Name the blood parasite species.
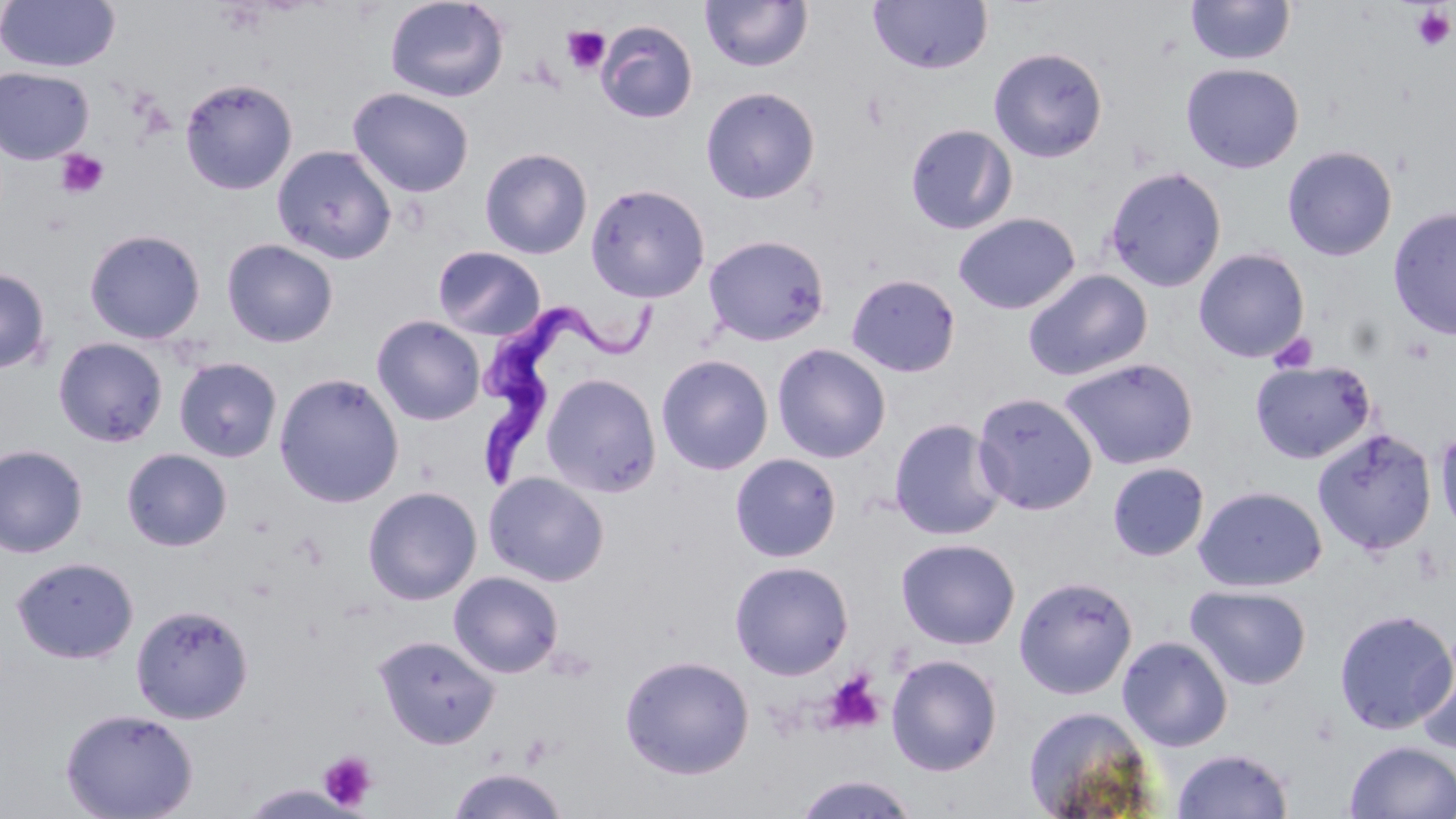
Trypanosoma brucei.

Approximate bounding boxes as (x1,y1)-(x2,y2) corner pairs in pixels. Trypanosoma brucei locations: (479,292)-(660,489). Platelet locations: (1411,6)-(1454,52), (562,26)-(610,74), (55,149)-(109,199), (1269,332)-(1318,374), (1400,337)-(1436,365), (819,670)-(886,736), (520,733)-(554,768), (318,750)-(378,811). Uninfected red blood cell locations: (0,0)-(121,73), (384,0)-(510,103), (700,0)-(812,73), (1186,0)-(1296,66), (868,1)-(992,75), (594,19)-(698,123), (988,47)-(1108,163), (1181,63)-(1304,173), (0,66)-(95,165), (179,77)-(298,195), (700,86)-(820,204), (348,87)-(475,198), (904,123)-(1018,235), (272,144)-(397,264), (1281,145)-(1398,261), (479,147)-(593,259), (1102,166)-(1228,292), (585,183)-(711,303), (1387,206)-(1456,340), (953,212)-(1081,314), (84,228)-(206,344), (702,234)-(831,347), (221,238)-(339,348), (432,246)-(547,341), (1193,248)-(1310,363), (0,267)-(51,374), (1023,269)-(1153,382), (845,272)-(961,378), (372,315)-(485,425), (53,336)-(168,447), (771,343)-(891,463), (656,354)-(774,475), (1058,356)-(1199,471), (173,357)-(283,463), (1249,359)-(1378,465), (274,372)-(404,508), (541,373)-(662,496), (971,391)-(1098,516), (887,417)-(1007,541), (1434,421)-(1456,541), (1311,427)-(1437,557), (0,444)-(88,558), (121,448)-(233,551), (729,452)-(842,562), (1107,461)-(1210,562), (483,472)-(610,587), (1193,485)-(1327,593), (362,486)-(482,606), (895,537)-(1021,650), (11,556)-(139,664), (729,560)-(854,680), (448,571)-(564,678), (1013,575)-(1139,700), (1185,584)-(1312,690), (131,603)-(254,724), (1333,608)-(1456,735), (1414,628)-(1456,756), (374,634)-(500,749), (1117,635)-(1234,751), (885,653)-(1003,777), (619,654)-(755,779), (1021,704)-(1156,818), (59,707)-(198,819), (1344,741)-(1456,818), (1171,747)-(1294,819), (446,767)-(570,819), (791,773)-(920,818). One field of a larger specimen. Captured at 1000x magnification. May-Grünwald-Giemsa stain. Optical microscopy. Thin blood smear. Image is 1456×819 pixels.